Report the malaria status of this cell.
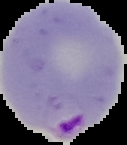
Parasitized.

image size = 127×145 pixels
image type = cell region segmented out of the field of view; surrounding area masked to black
preparation = thin blood smear